Report the malaria status of this cell.
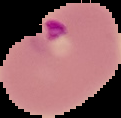
Parasitized.

Cell region segmented out of the field of view; the surrounding area is masked to black. From a thin blood film. Image is 121×118 pixels.